Give a bounding box for every leukocyte visible.
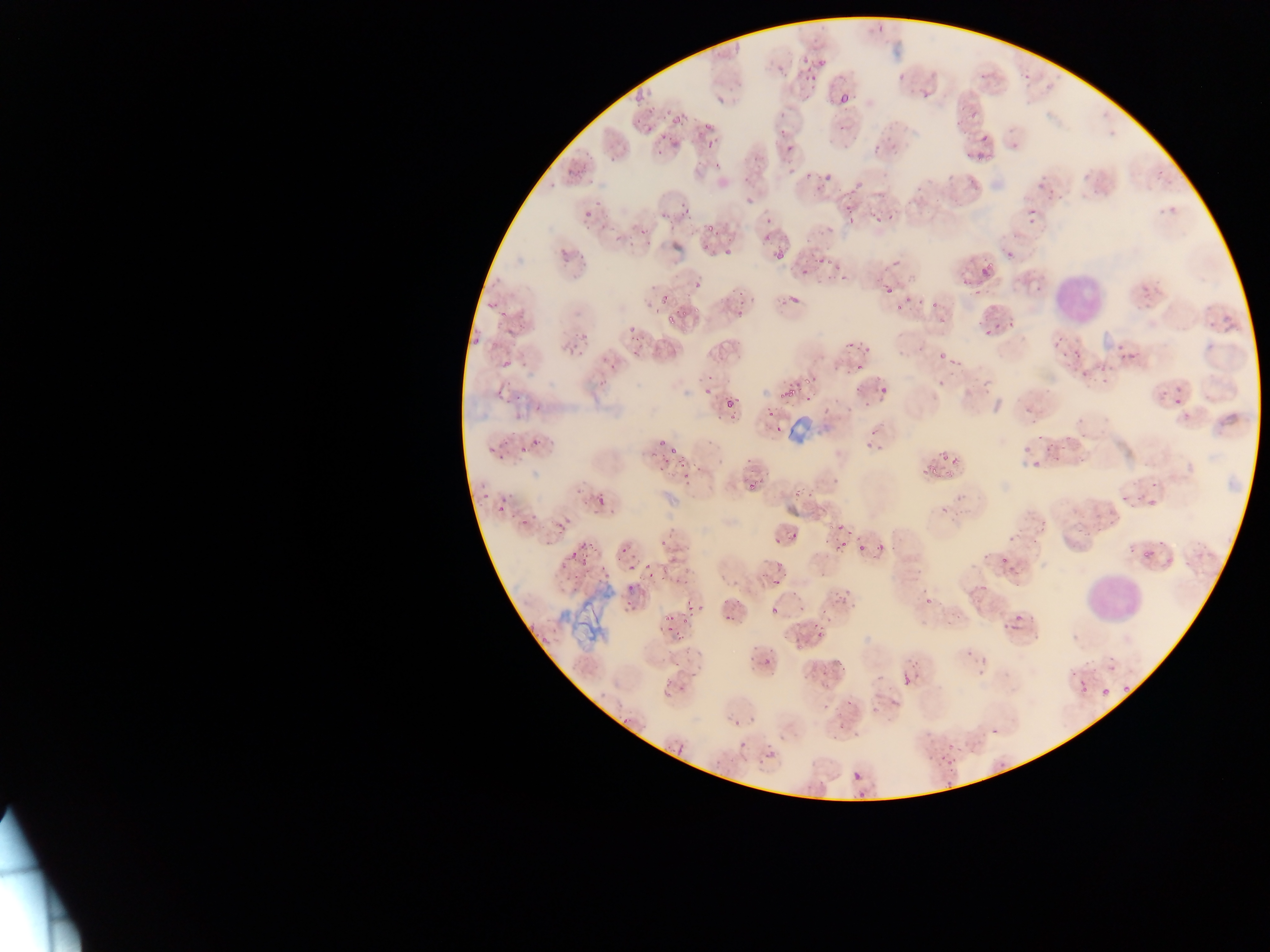

Approximate bounding boxes as {left, top, right, bottom} in pixels.
Leukocytes: {1051, 265, 1108, 325}, {1080, 565, 1149, 629}.

preparation: thin blood smear
capture: mobile-phone photograph through a microscope
image_size: 1270×952 pixels
malaria_parasite_locations: 'approximate bounding boxes as {left, top, right, bottom} in pixels: {875, 22, 886, 30}, {816, 49, 837, 65}, {801, 53, 812, 66}, {800, 66, 816, 81}, {896, 68, 908, 79}, {1021, 68, 1032, 83}, {920, 86, 934, 101}, {634, 89, 649, 98}, {837, 93, 851, 106}, {958, 99, 967, 112}, {971, 109, 983, 117}, {671, 112, 685, 120}, {775, 117, 796, 135}, {701, 118, 717, 130}, {643, 124, 657, 135}, {657, 133, 671, 149}, {704, 134, 717, 152}, {872, 135, 887, 152}, {978, 136, 988, 145}, {784, 137, 795, 154}, {962, 150, 971, 159}, {821, 175, 830, 186}, {595, 193, 600, 210}, {677, 199, 692, 216}, {843, 204, 852, 209}, {885, 206, 898, 219}, {583, 208, 594, 221}, {1025, 209, 1033, 216}, {705, 213, 716, 232}, {872, 213, 881, 224}, {1027, 215, 1040, 228}, {763, 218, 776, 222}, {846, 218, 855, 224}, {557, 242, 574, 256}, {725, 242, 736, 261}, {1005, 246, 1020, 257}, {770, 252, 782, 262}, {818, 254, 828, 263}, {835, 263, 847, 277}, {976, 264, 995, 285}, {798, 269, 808, 274}, {685, 274, 704, 293}, {882, 282, 891, 297}, {1141, 282, 1158, 294}, {659, 286, 673, 303}, {787, 291, 804, 309}, {932, 294, 944, 311}, {901, 295, 911, 306}, {482, 304, 491, 313}, {495, 305, 511, 318}, {886, 306, 898, 313}, {664, 309, 673, 324}, {980, 321, 1002, 341}, {624, 327, 634, 339}, {1051, 330, 1064, 351}, {578, 331, 591, 343}, {1113, 337, 1130, 363}, {468, 341, 480, 352}, {566, 341, 579, 355}, {845, 342, 851, 351}, {861, 345, 867, 356}, {1070, 345, 1089, 360}, {947, 355, 959, 364}, {607, 358, 620, 371}, {500, 359, 513, 372}, {853, 362, 864, 372}, {1101, 366, 1110, 373}, {806, 371, 818, 388}, {934, 379, 943, 388}, {874, 382, 893, 403}, {695, 383, 711, 403}, {779, 387, 796, 410}, {802, 388, 815, 399}, {1172, 388, 1186, 405}, {509, 390, 524, 401}, {724, 392, 739, 411}, {1025, 402, 1031, 411}, {766, 410, 775, 418}, {1079, 412, 1087, 426}, {724, 416, 737, 421}, {774, 426, 783, 431}, {1036, 433, 1051, 444}, {532, 435, 543, 447}, {863, 435, 872, 452}, {664, 442, 673, 449}, {875, 443, 884, 454}, {940, 443, 950, 458}, {647, 445, 656, 456}, {517, 447, 525, 456}, {671, 447, 682, 454}, {485, 448, 493, 457}, {495, 451, 508, 459}, {951, 455, 961, 466}, {1030, 456, 1045, 467}, {921, 462, 932, 477}, {656, 464, 665, 472}, {681, 475, 690, 482}, {748, 477, 758, 488}, {1147, 478, 1165, 490}, {497, 493, 510, 513}, {593, 494, 606, 510}, {1119, 494, 1130, 502}, {478, 495, 485, 504}, {940, 501, 949, 513}, {517, 511, 528, 530}, {834, 519, 848, 532}, {555, 521, 570, 533}, {790, 530, 798, 537}, {770, 534, 785, 549}, {660, 537, 671, 549}, {833, 537, 844, 548}, {575, 538, 588, 558}, {618, 542, 627, 559}, {876, 542, 885, 551}, {854, 544, 865, 553}, {996, 550, 1009, 565}, {1140, 550, 1147, 562}, {567, 553, 577, 562}, {623, 555, 638, 573}, {578, 556, 592, 568}, {1005, 562, 1016, 580}, {574, 565, 585, 578}, {642, 565, 657, 578}, {600, 568, 615, 581}, {771, 568, 786, 588}, {756, 572, 765, 579}, {674, 574, 683, 585}, {625, 584, 632, 593}, {925, 588, 936, 608}, {840, 590, 855, 603}, {621, 599, 633, 610}, {685, 600, 693, 609}, {794, 600, 806, 611}, {768, 602, 782, 612}, {697, 603, 706, 611}, {818, 605, 834, 617}, {668, 610, 676, 620}, {1014, 613, 1026, 628}, {722, 614, 732, 625}, {677, 619, 686, 628}, {1001, 622, 1016, 639}, {665, 625, 671, 634}, {537, 629, 551, 644}, {814, 629, 822, 638}, {960, 638, 978, 660}, {763, 650, 776, 667}, {671, 661, 684, 672}, {901, 667, 912, 685}, {820, 671, 828, 679}, {1072, 672, 1097, 701}, {1098, 679, 1111, 697}, {1121, 681, 1133, 695}, {661, 683, 670, 695}, {846, 694, 855, 706}, {891, 696, 901, 706}, {820, 697, 833, 710}, {621, 713, 631, 728}, {839, 716, 852, 728}, {990, 724, 1004, 735}, {738, 738, 754, 751}, {764, 745, 779, 762}, {938, 751, 951, 762}, {994, 757, 1008, 766}, {851, 770, 863, 783} | approximate {x, y} pixel centers of objects too small to bound: {765, 235}, {1085, 367}, {1162, 394}, {867, 407}'
country: Ghana
field_of_view: single